Give the position of every Plasmodium parasite.
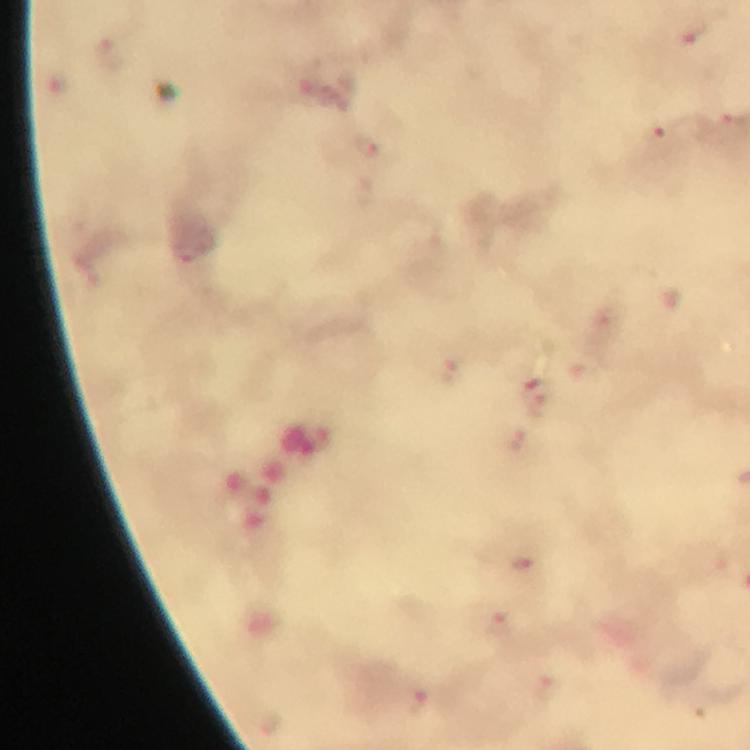
Approximate centers as (x, y) in pixels.
Plasmodium parasites: (691, 35), (659, 136), (368, 146), (185, 252), (446, 369), (539, 405), (522, 562), (500, 623), (416, 704).

A crop from one field of view. Giemsa stain. At 100x magnification. Immersion oil applied. Image is 750×750 pixels. Thick blood film. Photographed with a smartphone mounted on the microscope. From a malaria diagnostic workup.